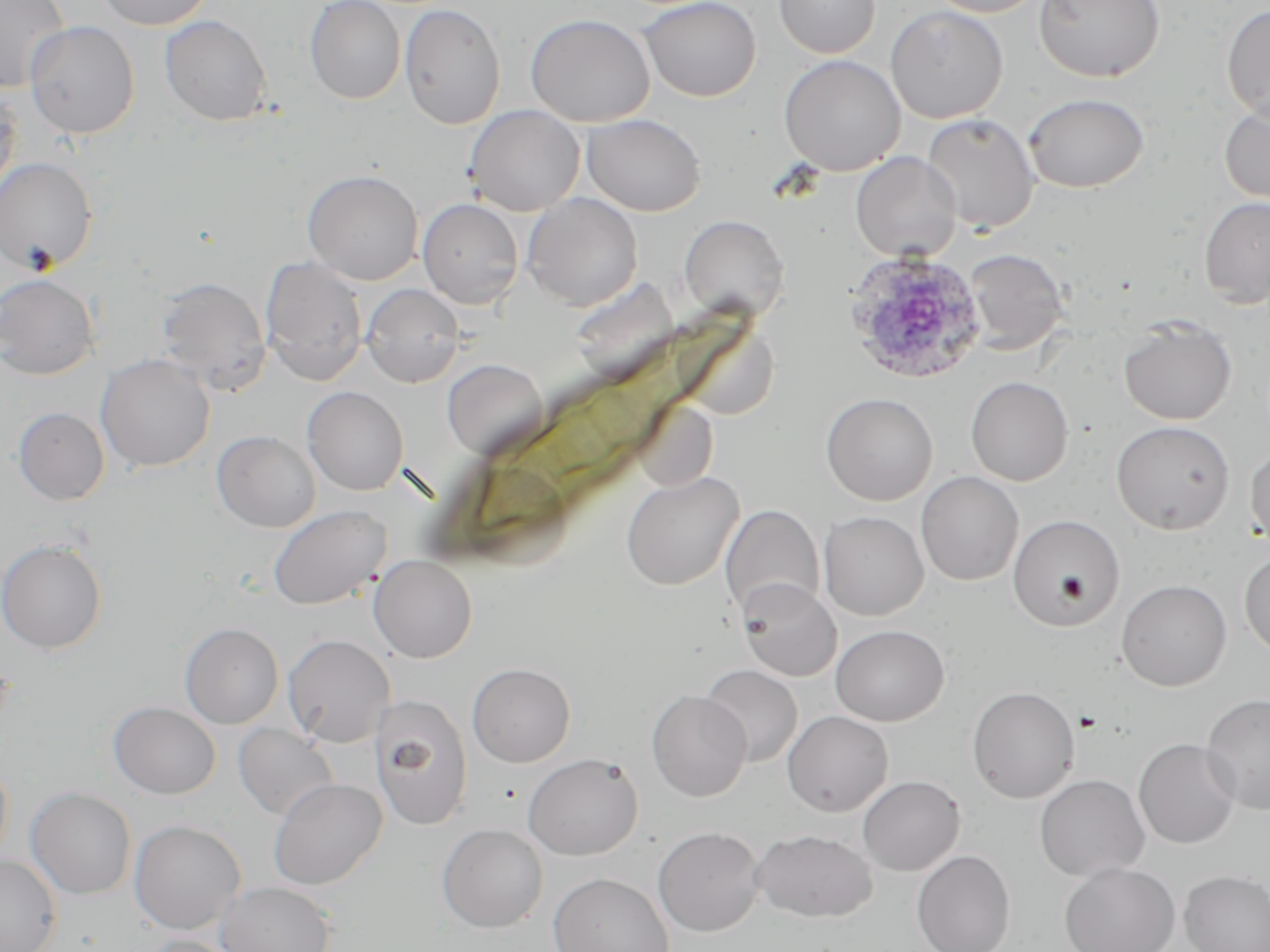
plasmodium_ovale_infected_red_blood_cell_locations: 'approximate bounding boxes as (x1,y1)-(x2,y2) corner pairs in pixels: (842,250)-(987,384)'
slide_level_diagnosis: Plasmodium ovale
image_size: 1270×952 pixels
field_of_view: one of a larger specimen
preparation: thin blood smear
magnification: 1000x
uninfected_red_blood_cell_locations: 'approximate bounding boxes as (x1,y1)-(x2,y2) corner pairs in pixels: (0,0)-(71,93), (95,0)-(215,29), (304,0)-(406,104), (638,0)-(762,101), (774,0)-(881,58), (923,0)-(1048,17), (1035,0)-(1165,82), (399,2)-(506,130), (885,4)-(1008,123), (1221,5)-(1270,124), (525,13)-(655,127), (160,15)-(273,126), (24,20)-(140,139), (778,54)-(905,176), (0,87)-(22,201), (1023,93)-(1150,192), (1219,98)-(1270,206), (463,105)-(585,216), (921,113)-(1039,233), (581,114)-(706,216), (850,152)-(961,261), (0,157)-(99,274), (302,170)-(423,285), (521,192)-(644,311), (1198,196)-(1270,308), (418,198)-(524,310), (678,215)-(789,321), (964,249)-(1069,355), (260,257)-(368,385), (0,273)-(100,380), (154,276)-(272,394), (361,284)-(464,387), (1118,316)-(1237,425), (96,353)-(215,472), (442,357)-(548,460), (965,376)-(1073,485), (302,386)-(408,495), (820,392)-(938,505), (631,399)-(719,492), (14,407)-(109,505), (1111,420)-(1235,534), (212,430)-(321,532), (1245,442)-(1270,548), (620,470)-(744,591), (915,471)-(1024,585), (268,504)-(391,610), (720,504)-(825,618), (818,511)-(929,621), (1007,514)-(1125,632), (0,537)-(108,654), (1239,549)-(1270,659), (369,554)-(478,663), (737,579)-(842,682), (1116,579)-(1232,691), (180,622)-(284,728), (830,624)-(949,726), (282,634)-(395,748), (467,663)-(575,767), (700,665)-(803,767), (967,686)-(1080,803), (647,690)-(751,801), (1201,694)-(1270,815), (369,695)-(474,830), (108,701)-(221,799), (782,710)-(893,816), (233,723)-(339,821), (1133,738)-(1240,849), (523,753)-(643,861), (0,756)-(13,870), (1034,774)-(1150,882), (857,775)-(965,876), (268,777)-(387,890), (26,787)-(136,899), (129,820)-(247,934), (437,823)-(548,933), (652,826)-(765,937), (751,828)-(878,922), (911,850)-(1016,952), (0,855)-(62,952), (1059,862)-(1180,952), (1179,870)-(1270,952), (548,872)-(674,952), (216,881)-(337,952), (138,934)-(251,952)'
modality: optical microscopy
stain: May-Grünwald-Giemsa